Describe the morphology of the erythrocytes.
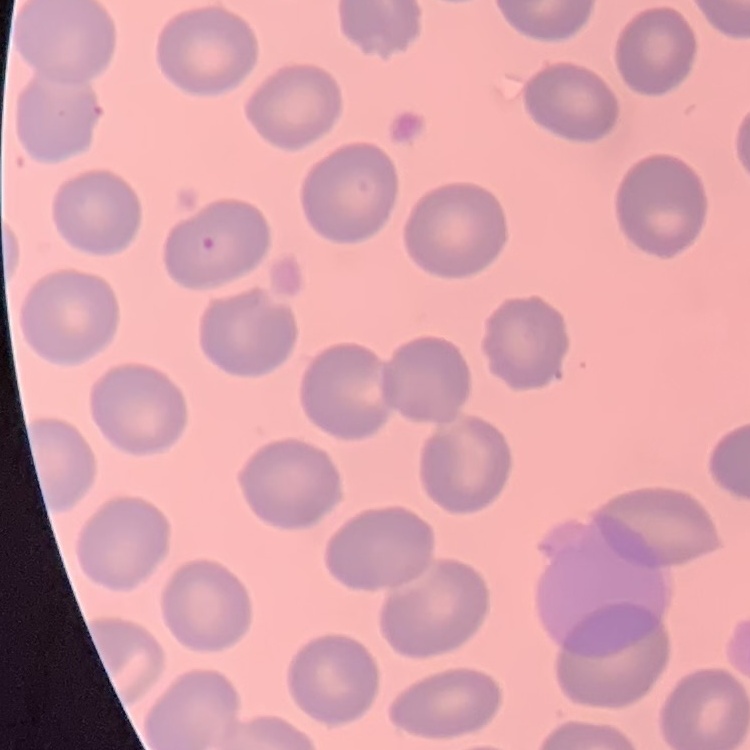

No rouleaux formation.

stain: Field's or Giemsa
preparation: thin blood smear
image_type: one tile cut from a larger photomicrograph